Outline each white blood cell.
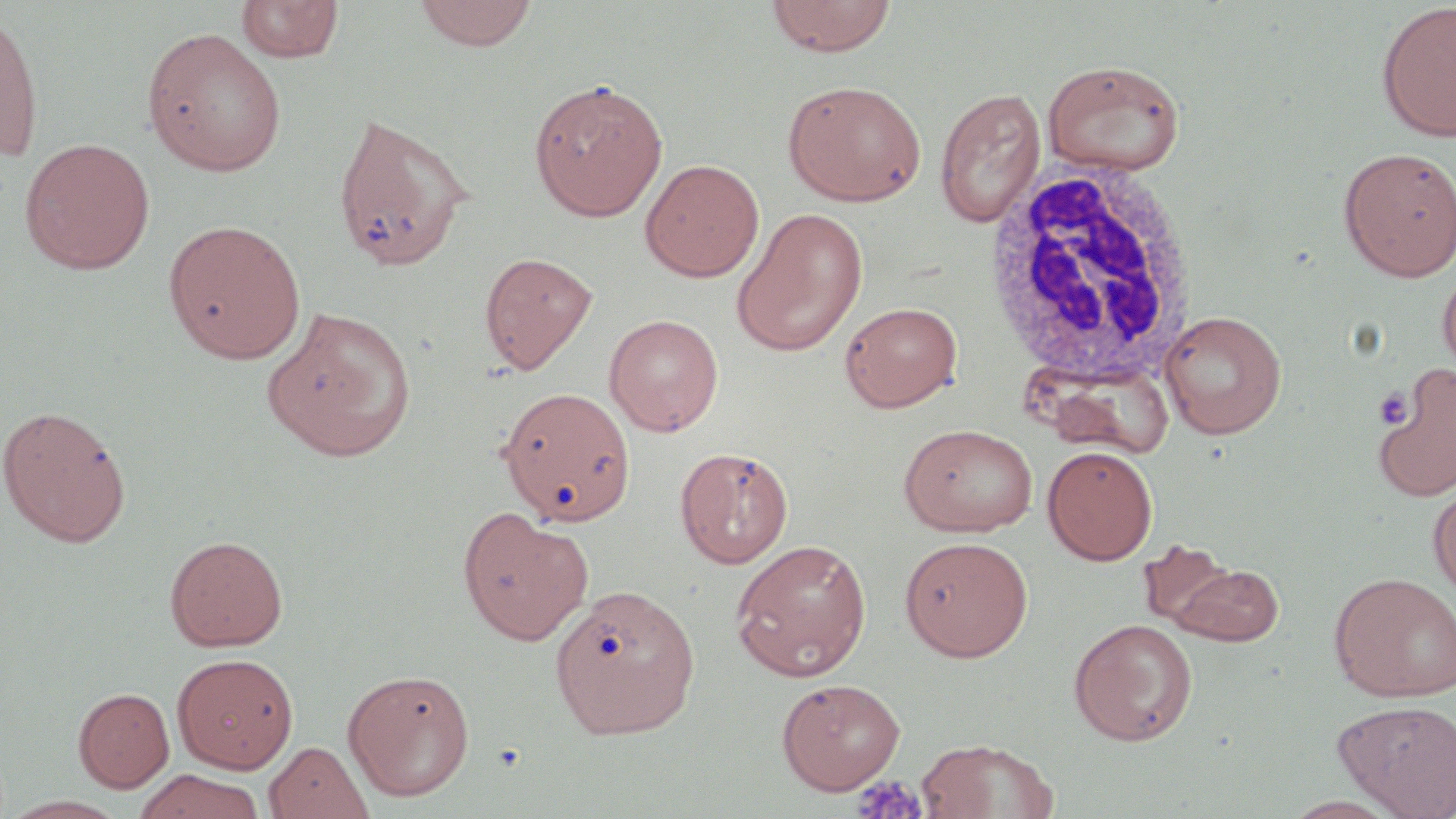

Approximate bounding boxes as (x1,y1)-(x2,y2) corner pairs in pixels.
White blood cells: (980,163)-(1200,391).

slide-level diagnosis = negative for blood parasites
platelet locations = approximate bounding boxes as (x1,y1)-(x2,y2) corner pairs in pixels: (1373,389)-(1413,428), (850,774)-(928,819)
uninfected red blood cell locations = approximate bounding boxes as (x1,y1)-(x2,y2) corner pairs in pixels: (236,0)-(344,63), (413,0)-(538,51), (764,0)-(897,56), (1376,3)-(1456,142), (0,5)-(44,164), (142,26)-(288,176), (1042,58)-(1187,176), (529,77)-(668,221), (782,79)-(927,206), (934,87)-(1046,228), (331,111)-(478,274), (19,137)-(155,274), (1338,146)-(1456,282), (640,158)-(764,282), (731,207)-(868,356), (163,219)-(306,363), (479,251)-(597,374), (1437,265)-(1456,381), (839,300)-(962,412), (263,306)-(418,462), (1159,309)-(1287,438), (603,313)-(724,436), (1372,366)-(1456,502), (499,389)-(637,528), (0,405)-(132,547), (898,422)-(1038,537), (1042,444)-(1158,565), (675,446)-(794,568), (1428,487)-(1456,599), (457,506)-(594,645), (164,534)-(288,651), (899,536)-(1033,661), (730,538)-(872,681), (1137,540)-(1246,636), (1166,560)-(1285,646), (1328,571)-(1456,702), (551,584)-(700,739), (1069,618)-(1198,746), (172,652)-(299,773), (342,667)-(476,802), (776,678)-(906,794), (73,687)-(174,792), (1333,699)-(1456,817), (914,738)-(1060,819), (265,741)-(373,819), (133,769)-(267,819)
preparation = thin blood smear
magnification = 1000x
stain = May-Grünwald-Giemsa
modality = light microscopy
image size = 1456×819 pixels
field of view = one of a larger specimen